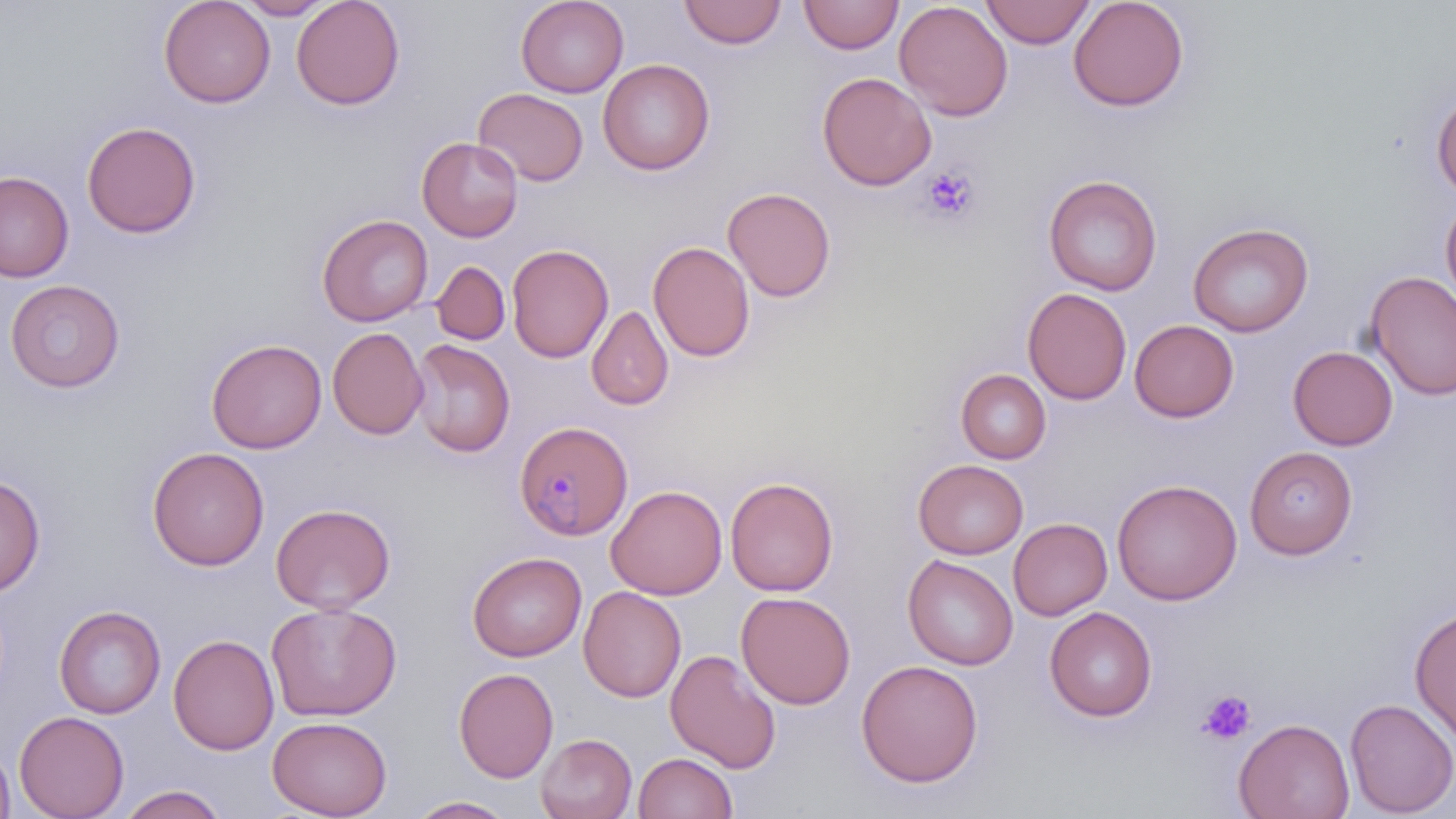

Approximate bounding boxes as (x1, y1, x2, y2) in pixels. Platelet locations: (920, 165, 980, 223), (1197, 691, 1256, 744). Uninfected red blood cell locations: (158, 0, 275, 108), (235, 0, 336, 20), (291, 0, 405, 110), (516, 0, 629, 97), (798, 0, 903, 54), (980, 0, 1095, 48), (1068, 0, 1189, 112), (678, 1, 787, 48), (893, 1, 1013, 121), (598, 59, 715, 175), (817, 71, 937, 191), (474, 88, 589, 186), (1432, 91, 1456, 198), (82, 121, 201, 238), (417, 137, 523, 242), (0, 171, 74, 282), (1043, 174, 1163, 296), (722, 186, 836, 302), (1440, 195, 1456, 315), (317, 213, 433, 326), (1188, 223, 1313, 336), (648, 241, 755, 362), (506, 243, 614, 363), (431, 261, 510, 345), (1364, 271, 1456, 401), (5, 279, 125, 392), (1022, 287, 1132, 405), (1023, 303, 1239, 410), (587, 305, 674, 410), (1129, 319, 1239, 422), (327, 327, 428, 440), (206, 338, 327, 453), (410, 339, 515, 457), (1288, 345, 1398, 450), (956, 369, 1051, 464), (1244, 445, 1358, 559), (147, 447, 269, 571), (913, 459, 1028, 559), (0, 474, 45, 596), (725, 476, 838, 596), (1111, 478, 1243, 605), (606, 484, 727, 599), (271, 502, 395, 614), (1008, 517, 1112, 620), (466, 551, 586, 661), (903, 554, 1018, 670), (578, 586, 686, 702), (736, 591, 856, 709), (266, 602, 402, 721), (54, 605, 166, 718), (1044, 606, 1157, 721), (1410, 607, 1456, 744), (168, 633, 279, 756), (665, 649, 781, 773), (856, 659, 984, 786), (453, 667, 559, 783), (1345, 697, 1456, 817), (14, 710, 129, 819), (267, 716, 392, 818), (1234, 717, 1355, 819), (535, 733, 637, 819), (0, 741, 15, 819), (633, 752, 738, 819), (116, 785, 229, 819), (407, 796, 517, 818). Plasmodium malariae-infected red blood cell locations: (514, 420, 632, 541). Slide-level diagnosis: Plasmodium malariae. Single field of view. 1000x magnification. Image is 1456×819 pixels. May-Grünwald-Giemsa-stained preparation. Optical microscopy. Thin blood film.